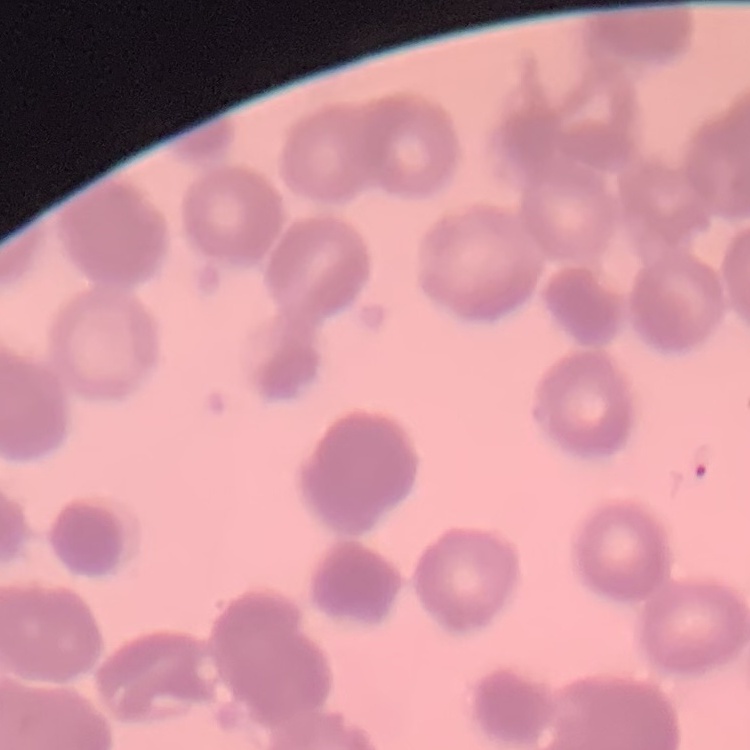
Summary:
  - Erythrocyte morphology: rouleaux formation
  - Preparation: thin blood smear
  - Stain: Field's or Giemsa
  - Image type: one tile cut from a larger photomicrograph